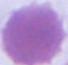

{
  "magnification": "1000x",
  "identification": "red blood cell",
  "modality": "photomicrograph"
}